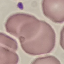
Summary:
  - Malaria status: uninfected
  - Image type: cell patch, automatically extracted from a larger field of view and resized to 64 × 64 pixels
  - Stain: Giemsa
  - Preparation: thin blood film
  - Capture: smartphone through the microscope eyepiece